Name the parasite shown.
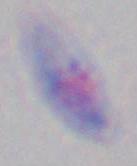
This is Toxoplasma gondii.

modality = micrograph
magnification = 1000x